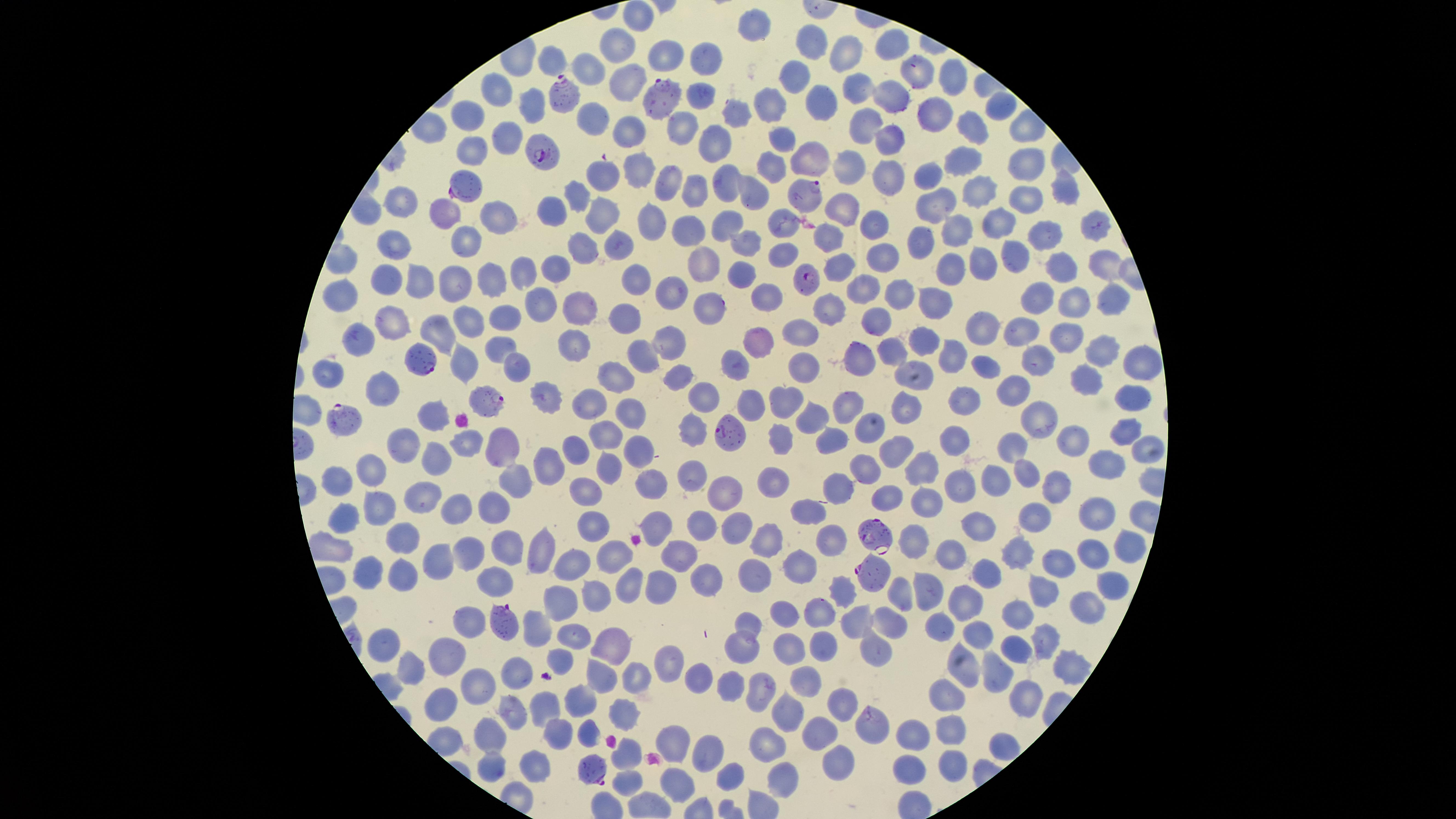
Approximate marker points, in pixels from the top-left corner. Uninfected red blood cells: (x=640, y=16), (x=758, y=28), (x=888, y=45), (x=618, y=46), (x=814, y=46), (x=666, y=53), (x=853, y=55), (x=711, y=59), (x=550, y=65), (x=920, y=75), (x=953, y=80), (x=629, y=84), (x=801, y=84), (x=853, y=84), (x=501, y=90), (x=890, y=92), (x=702, y=96), (x=535, y=101), (x=1000, y=104), (x=770, y=105), (x=818, y=105), (x=932, y=108), (x=738, y=112), (x=468, y=118), (x=872, y=123), (x=678, y=126), (x=629, y=127), (x=974, y=127), (x=785, y=136), (x=719, y=140), (x=891, y=140), (x=503, y=141), (x=466, y=153), (x=814, y=157), (x=964, y=160), (x=1018, y=162), (x=775, y=165), (x=847, y=166), (x=639, y=167), (x=605, y=172), (x=929, y=176), (x=725, y=177), (x=892, y=179), (x=665, y=182), (x=695, y=187), (x=1059, y=188), (x=977, y=191), (x=576, y=193), (x=754, y=193), (x=1021, y=202), (x=557, y=203), (x=938, y=204), (x=405, y=205), (x=843, y=207), (x=603, y=211), (x=450, y=214), (x=497, y=215), (x=646, y=217), (x=784, y=218), (x=880, y=222), (x=993, y=222), (x=723, y=224), (x=1087, y=226), (x=693, y=228), (x=955, y=228), (x=1043, y=236), (x=465, y=237), (x=832, y=237), (x=747, y=241), (x=919, y=243), (x=393, y=245), (x=584, y=245), (x=619, y=247), (x=780, y=252), (x=881, y=253), (x=984, y=254), (x=1010, y=254), (x=553, y=261), (x=707, y=261), (x=1105, y=262), (x=842, y=266), (x=945, y=267), (x=1061, y=267), (x=742, y=268), (x=521, y=274), (x=634, y=276), (x=422, y=281), (x=388, y=283), (x=456, y=285), (x=496, y=285), (x=669, y=290), (x=862, y=290), (x=764, y=293), (x=898, y=293), (x=342, y=295), (x=1037, y=298), (x=1111, y=299), (x=1071, y=301), (x=538, y=302), (x=935, y=304), (x=585, y=307), (x=708, y=307), (x=832, y=308), (x=629, y=317), (x=880, y=318), (x=471, y=320), (x=508, y=322), (x=396, y=323), (x=804, y=329), (x=984, y=329), (x=439, y=330), (x=1021, y=331), (x=915, y=335), (x=1065, y=336), (x=578, y=340), (x=756, y=342), (x=361, y=344), (x=500, y=344), (x=671, y=344), (x=891, y=345), (x=1098, y=351), (x=951, y=355), (x=857, y=358), (x=644, y=359), (x=514, y=361), (x=740, y=361), (x=984, y=363), (x=1142, y=364), (x=804, y=366), (x=1034, y=367), (x=463, y=368), (x=324, y=373), (x=614, y=373), (x=681, y=375), (x=920, y=376), (x=1086, y=382), (x=385, y=388), (x=1012, y=390), (x=967, y=394), (x=705, y=395), (x=544, y=398), (x=787, y=398), (x=1135, y=398), (x=591, y=399), (x=847, y=405), (x=902, y=406), (x=435, y=413), (x=629, y=417), (x=1039, y=418), (x=813, y=420), (x=694, y=429), (x=866, y=429), (x=1124, y=431), (x=604, y=434), (x=829, y=436), (x=948, y=438), (x=405, y=442), (x=778, y=442), (x=1073, y=442), (x=468, y=444), (x=507, y=444), (x=897, y=445), (x=1016, y=446), (x=1144, y=446), (x=575, y=447), (x=634, y=449), (x=435, y=457), (x=552, y=460), (x=1106, y=461), (x=611, y=464), (x=917, y=464), (x=862, y=468), (x=690, y=472), (x=1026, y=472), (x=377, y=473), (x=511, y=477), (x=997, y=478), (x=774, y=479), (x=339, y=482), (x=648, y=482), (x=1060, y=484), (x=724, y=485), (x=839, y=485), (x=963, y=486), (x=585, y=493), (x=422, y=494), (x=887, y=499), (x=455, y=504), (x=493, y=509), (x=811, y=509), (x=1039, y=512), (x=1092, y=513), (x=345, y=515), (x=377, y=516), (x=983, y=519), (x=735, y=523), (x=693, y=525), (x=592, y=526), (x=661, y=529), (x=769, y=533), (x=831, y=540), (x=401, y=541), (x=467, y=546), (x=509, y=546), (x=544, y=547), (x=1121, y=547), (x=951, y=549), (x=1015, y=549), (x=1094, y=552), (x=1058, y=558), (x=619, y=559), (x=679, y=560), (x=432, y=561), (x=796, y=561), (x=568, y=562), (x=760, y=569), (x=983, y=570), (x=366, y=574), (x=401, y=580), (x=709, y=580), (x=1112, y=580), (x=497, y=582), (x=663, y=585), (x=1040, y=585), (x=631, y=590), (x=841, y=591), (x=902, y=591), (x=927, y=594), (x=600, y=596), (x=558, y=598), (x=968, y=600), (x=1090, y=602), (x=785, y=608), (x=821, y=612), (x=1019, y=612), (x=893, y=617), (x=858, y=618), (x=749, y=621), (x=471, y=622), (x=944, y=623), (x=531, y=627), (x=982, y=634), (x=575, y=637), (x=1045, y=637), (x=1020, y=641), (x=383, y=643), (x=825, y=643), (x=616, y=645), (x=880, y=645), (x=739, y=647), (x=793, y=649), (x=454, y=653), (x=558, y=656), (x=663, y=660), (x=1073, y=662), (x=410, y=665), (x=964, y=666), (x=997, y=669), (x=518, y=670), (x=602, y=672), (x=697, y=676), (x=809, y=676), (x=634, y=677), (x=479, y=684), (x=730, y=684), (x=757, y=692), (x=1024, y=693), (x=945, y=694), (x=441, y=699), (x=578, y=700), (x=790, y=703), (x=840, y=704), (x=545, y=705), (x=627, y=708), (x=514, y=717), (x=819, y=728), (x=560, y=729), (x=587, y=729), (x=869, y=729), (x=944, y=733), (x=489, y=734), (x=908, y=737), (x=680, y=739), (x=769, y=742), (x=704, y=746), (x=998, y=747), (x=627, y=756), (x=950, y=764), (x=839, y=765), (x=490, y=766), (x=536, y=767), (x=735, y=774), (x=905, y=775), (x=785, y=776), (x=679, y=781), (x=626, y=783). Parasitized red blood cells: (x=566, y=92), (x=674, y=97), (x=544, y=154), (x=461, y=186), (x=807, y=195), (x=805, y=281), (x=423, y=358), (x=486, y=398), (x=338, y=417), (x=728, y=435), (x=873, y=535), (x=871, y=572), (x=500, y=623), (x=593, y=769). Image is 1456×819 pixels. Presence: malaria parasites identified. Giemsa stain. Thin blood film. Smartphone photograph through the microscope eyepiece. Circular visible region. One field of view of the specimen. Species: Plasmodium falciparum.